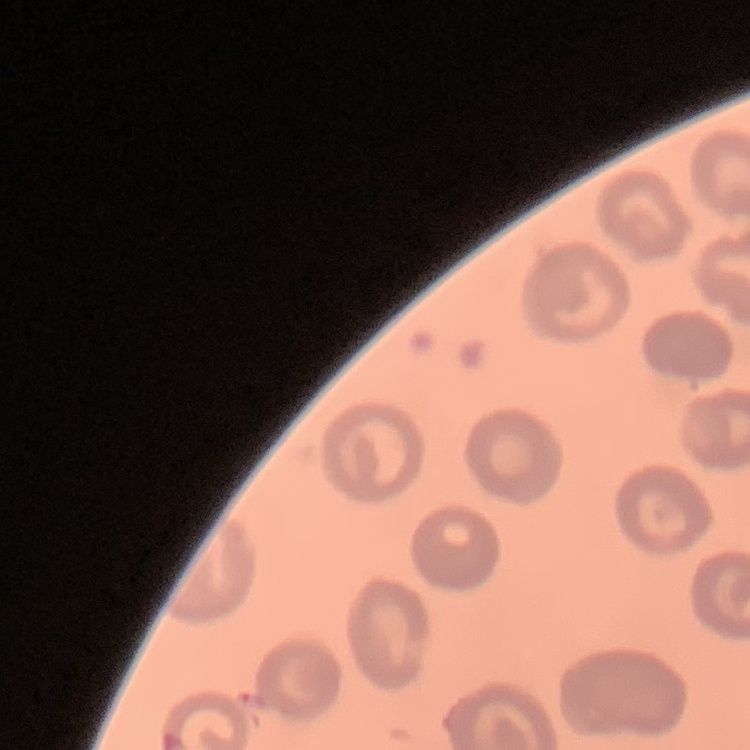

Summary:
  - Erythrocyte morphology: no rouleaux formation
  - Preparation: thin peripheral smear
  - Stain: Field's or Giemsa
  - Image type: square crop of a larger photomicrograph